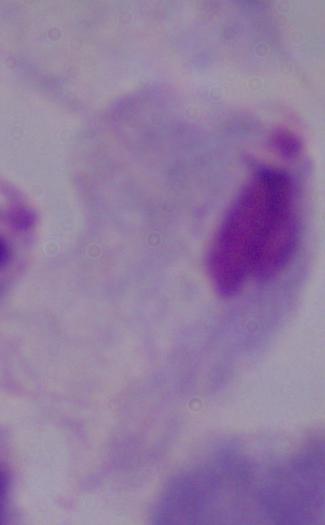
Summary:
  - Magnification: 1000x
  - Modality: photomicrograph
  - Identification: trichomonad